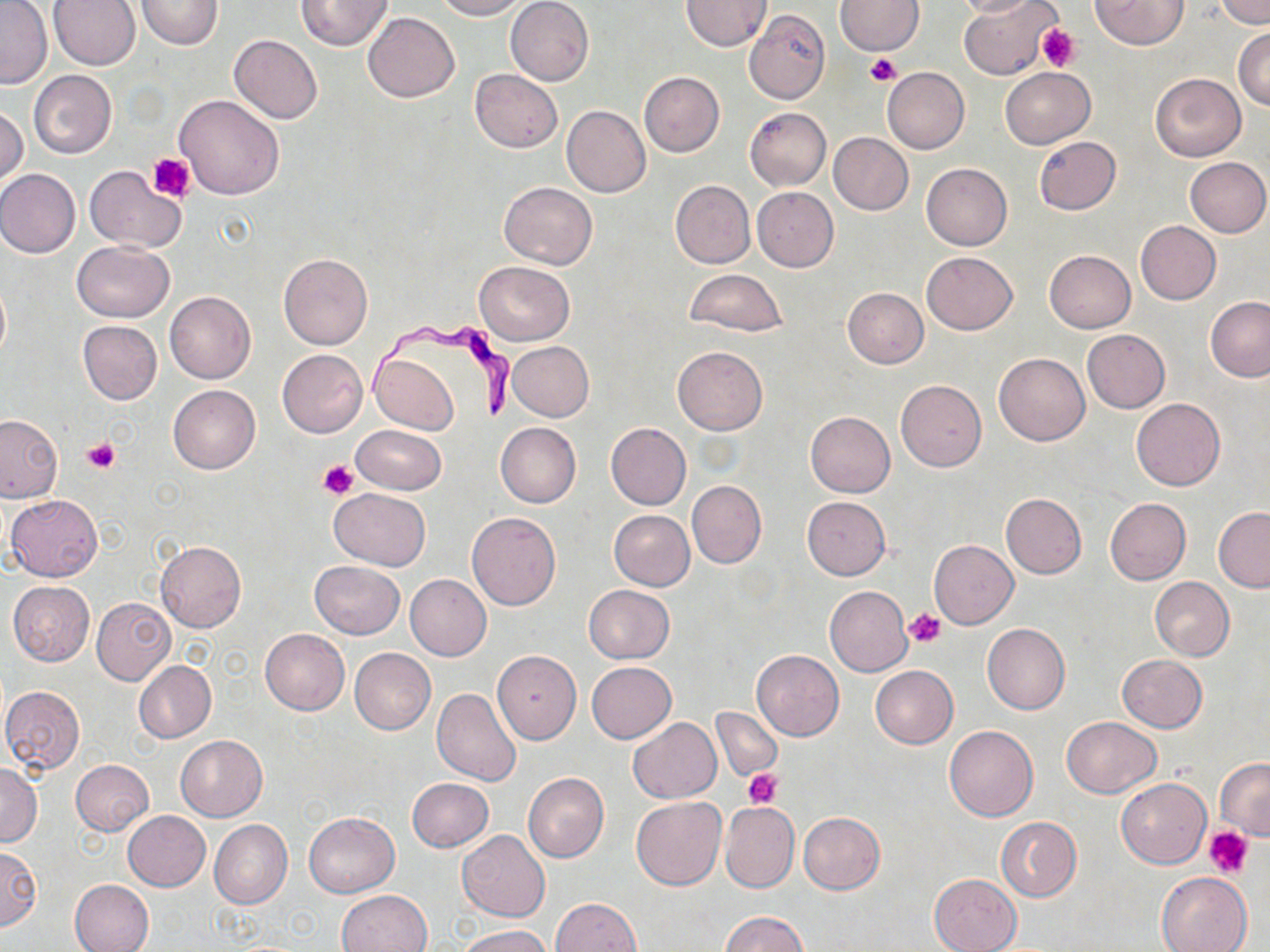

Summary:
  - Coordinate format: approximate bounding boxes as (x1, y1, x2, y2) in pixels
  - Trypanosoma brucei locations: (362, 312, 519, 423)
  - Uninfected red blood cell locations: (136, 0, 223, 50), (296, 0, 391, 51), (433, 0, 527, 20), (834, 0, 924, 55), (954, 0, 1038, 18), (958, 0, 1056, 80), (1090, 0, 1188, 50), (1218, 0, 1268, 27), (0, 1, 51, 88), (48, 1, 139, 71), (505, 1, 593, 86), (680, 1, 772, 51), (743, 10, 830, 105), (363, 12, 459, 103), (1233, 27, 1270, 110), (229, 34, 323, 123), (881, 67, 969, 154), (1001, 67, 1094, 148), (470, 69, 562, 153), (28, 70, 117, 159), (639, 71, 724, 157), (1150, 73, 1245, 161), (173, 94, 285, 200), (1, 104, 27, 189), (562, 106, 651, 197), (745, 107, 831, 190), (829, 132, 913, 215), (1034, 136, 1121, 214), (1185, 157, 1270, 236), (921, 163, 1012, 250), (84, 165, 186, 252), (0, 170, 81, 258), (671, 181, 755, 268), (499, 182, 598, 269), (752, 186, 839, 271), (1135, 220, 1221, 305), (71, 241, 174, 322), (1044, 249, 1135, 332), (922, 251, 1018, 334), (278, 253, 372, 349), (474, 261, 574, 345), (684, 268, 788, 337), (842, 288, 928, 369), (164, 291, 255, 384), (1205, 297, 1270, 382), (77, 321, 162, 405), (1082, 329, 1170, 413), (508, 342, 594, 421), (672, 346, 767, 435), (278, 349, 367, 437), (369, 352, 458, 435), (995, 353, 1090, 445), (895, 379, 986, 471), (169, 384, 260, 473), (1131, 398, 1225, 490), (805, 411, 895, 497), (0, 414, 63, 502), (496, 423, 580, 508), (605, 423, 690, 510), (352, 425, 446, 495), (686, 480, 766, 569), (318, 489, 415, 643), (328, 489, 430, 569), (1001, 493, 1086, 578), (4, 494, 103, 581), (802, 497, 891, 579), (1104, 498, 1191, 584), (1213, 507, 1270, 592), (609, 510, 696, 591), (467, 513, 561, 610), (929, 540, 1017, 628), (156, 541, 246, 633), (310, 560, 404, 638), (405, 575, 491, 660), (1150, 577, 1234, 660), (8, 581, 95, 666), (582, 585, 676, 663), (824, 586, 912, 676), (90, 598, 175, 685), (981, 623, 1071, 715), (260, 628, 350, 715), (350, 648, 435, 735), (752, 650, 844, 740), (491, 651, 582, 744), (1117, 654, 1208, 733), (134, 661, 216, 743), (586, 661, 676, 743), (870, 665, 958, 749), (1, 686, 86, 773), (433, 688, 522, 786), (711, 706, 782, 781), (628, 717, 722, 802), (1061, 717, 1161, 798), (944, 725, 1038, 822), (176, 735, 266, 821), (1216, 758, 1270, 840), (71, 759, 153, 835), (0, 764, 42, 846), (523, 772, 609, 862), (406, 778, 493, 852), (1116, 778, 1211, 868), (631, 797, 726, 890), (719, 801, 799, 892), (123, 811, 210, 891), (305, 812, 400, 896), (798, 812, 886, 894), (994, 816, 1081, 903), (209, 819, 292, 909), (457, 831, 550, 921), (0, 846, 41, 931), (1155, 872, 1252, 952), (929, 873, 1022, 952), (70, 879, 155, 952), (338, 890, 431, 952), (552, 898, 641, 952), (721, 911, 806, 951), (461, 924, 550, 951)
  - Platelet locations: (1036, 25, 1079, 72), (866, 53, 902, 87), (149, 153, 195, 202), (84, 438, 120, 473), (317, 460, 358, 500), (904, 608, 945, 648), (744, 769, 783, 809), (1206, 826, 1254, 876)
  - Slide-level diagnosis: Trypanosoma brucei
  - Stain: May-Grünwald-Giemsa
  - Magnification: 1000x
  - Image size: 1270×952 pixels
  - Field of view: one of a larger specimen
  - Modality: optical microscopy
  - Preparation: thin blood film